Assess the morphology of the erythrocytes.
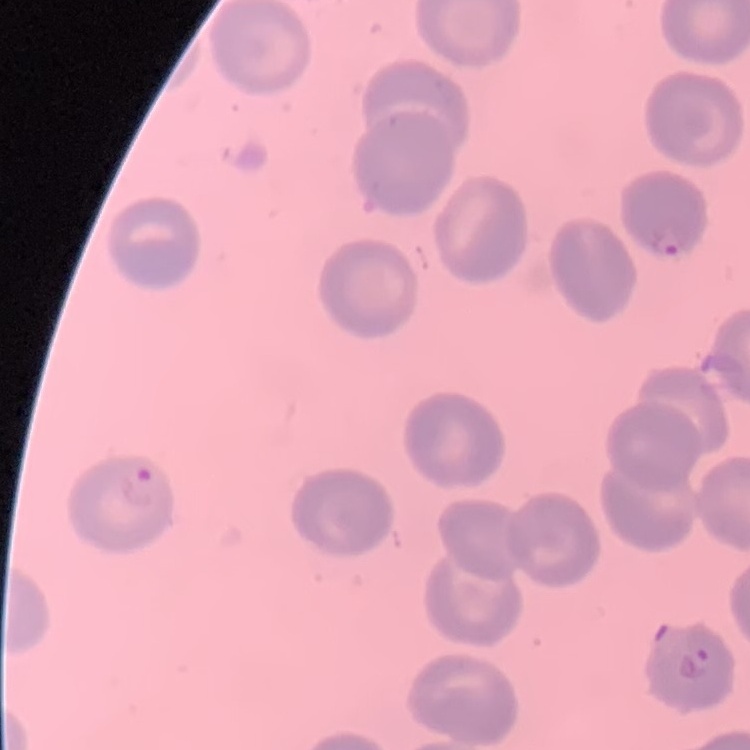

They show no rouleaux formation.

Summary:
  - Image type: square crop of a larger photomicrograph
  - Stain: Field's or Giemsa
  - Preparation: thin blood film